Report the malaria status of this cell.
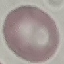
Uninfected.

Thin blood film. Automatically extracted cell patch, resized to 64 × 64 pixels. Giemsa stain. Acquired by smartphone through the microscope eyepiece.